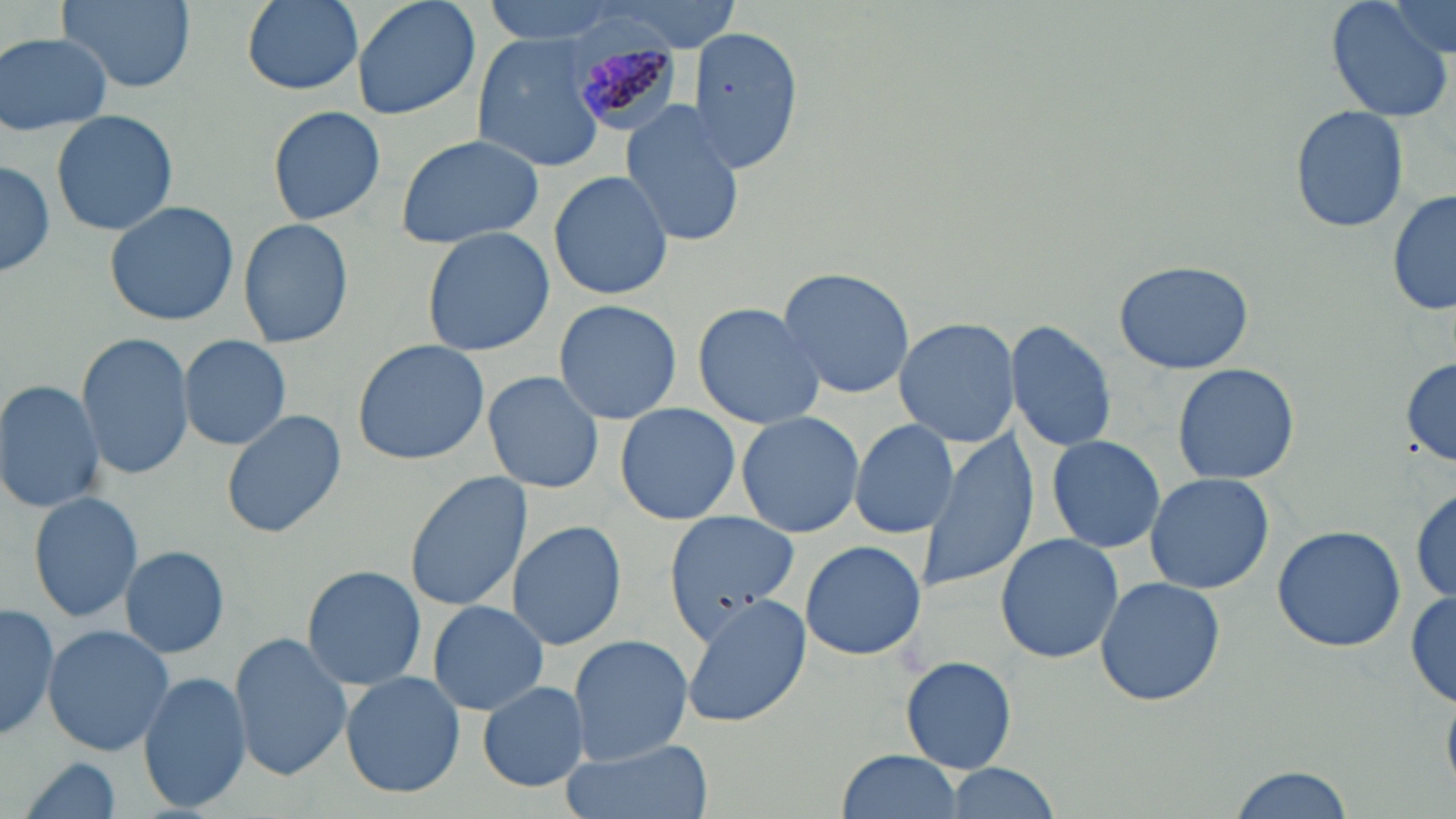
Summary:
  - Coordinate format: approximate bounding boxes as named x1/y1/x2/y2 corners in pixels
  - Plasmodium malariae-infected red blood cell locations: (x1=566, y1=30, x2=686, y2=139)
  - Uninfected red blood cell locations: (x1=239, y1=0, x2=364, y2=95), (x1=350, y1=0, x2=482, y2=120), (x1=481, y1=0, x2=628, y2=44), (x1=1325, y1=0, x2=1456, y2=124), (x1=1383, y1=0, x2=1453, y2=58), (x1=58, y1=1, x2=193, y2=93), (x1=584, y1=1, x2=747, y2=49), (x1=690, y1=24, x2=804, y2=173), (x1=1, y1=34, x2=115, y2=135), (x1=471, y1=34, x2=609, y2=171), (x1=620, y1=99, x2=743, y2=248), (x1=1289, y1=103, x2=1411, y2=234), (x1=264, y1=104, x2=389, y2=227), (x1=50, y1=109, x2=180, y2=237), (x1=394, y1=134, x2=548, y2=250), (x1=0, y1=160, x2=57, y2=280), (x1=549, y1=170, x2=673, y2=301), (x1=1388, y1=188, x2=1455, y2=320), (x1=105, y1=201, x2=239, y2=325), (x1=237, y1=218, x2=356, y2=350), (x1=421, y1=227, x2=554, y2=356), (x1=1114, y1=257, x2=1255, y2=375), (x1=776, y1=267, x2=917, y2=397), (x1=553, y1=300, x2=682, y2=425), (x1=691, y1=302, x2=825, y2=429), (x1=893, y1=318, x2=1018, y2=447), (x1=1005, y1=320, x2=1117, y2=453), (x1=76, y1=332, x2=192, y2=481), (x1=180, y1=335, x2=292, y2=450), (x1=350, y1=339, x2=488, y2=466), (x1=1400, y1=358, x2=1455, y2=467), (x1=1171, y1=361, x2=1299, y2=484), (x1=483, y1=371, x2=604, y2=495), (x1=0, y1=380, x2=106, y2=512), (x1=614, y1=403, x2=741, y2=526), (x1=222, y1=409, x2=346, y2=539), (x1=735, y1=411, x2=864, y2=538), (x1=848, y1=418, x2=956, y2=538), (x1=915, y1=429, x2=1038, y2=590), (x1=1045, y1=435, x2=1165, y2=552), (x1=405, y1=470, x2=533, y2=612), (x1=1144, y1=472, x2=1276, y2=595), (x1=1410, y1=484, x2=1456, y2=603), (x1=27, y1=489, x2=144, y2=622), (x1=662, y1=508, x2=803, y2=644), (x1=507, y1=520, x2=626, y2=651), (x1=1271, y1=525, x2=1406, y2=651), (x1=995, y1=534, x2=1124, y2=663), (x1=800, y1=540, x2=927, y2=662), (x1=119, y1=545, x2=229, y2=659), (x1=297, y1=564, x2=428, y2=693), (x1=1094, y1=574, x2=1226, y2=706), (x1=1407, y1=588, x2=1456, y2=709), (x1=679, y1=597, x2=811, y2=728), (x1=0, y1=600, x2=60, y2=742), (x1=426, y1=600, x2=549, y2=715), (x1=42, y1=625, x2=175, y2=757), (x1=228, y1=633, x2=351, y2=783), (x1=567, y1=636, x2=693, y2=766), (x1=900, y1=653, x2=1019, y2=773), (x1=139, y1=672, x2=252, y2=812), (x1=341, y1=672, x2=464, y2=798), (x1=477, y1=681, x2=590, y2=793), (x1=561, y1=737, x2=713, y2=819), (x1=836, y1=749, x2=963, y2=819), (x1=15, y1=755, x2=127, y2=819), (x1=938, y1=764, x2=1062, y2=819), (x1=1226, y1=766, x2=1354, y2=819)
  - Slide-level diagnosis: Plasmodium malariae
  - Preparation: thin blood smear
  - Field of view: single
  - Image size: 1456×819 pixels
  - Stain: May-Grünwald-Giemsa
  - Modality: optical microscopy
  - Magnification: 1000x